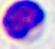 400x magnification. Micrograph. A leukocyte is shown.